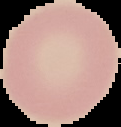

Summary:
  - Image size: 121×127 pixels
  - Malaria status: uninfected
  - Image type: segmented cell region on a black background
  - Preparation: thin blood film